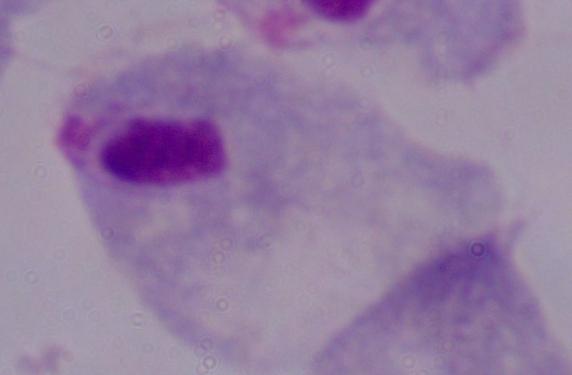

Captured at 1000x magnification. Micrograph. A trichomonad is seen.